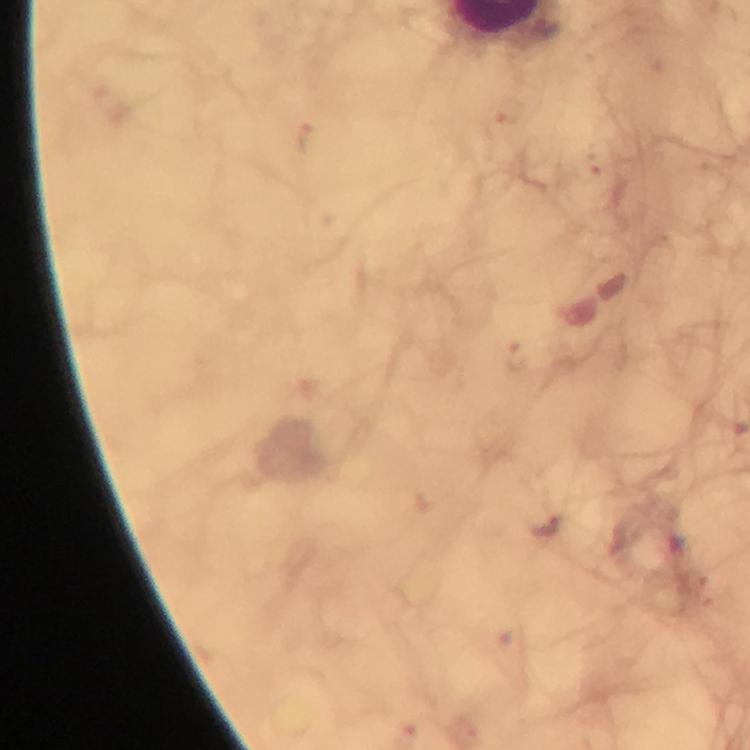
magnification = 100x
Plasmodium parasite locations = approximate object centers, in pixels from the top-left corner: (x=545, y=525)
stain = Giemsa
context = from a malaria diagnostic workup
capture = smartphone camera through the microscope
preparation = thick smear
image size = 750×750 pixels
immersion oil = used
cropped from = a single field of view